Classify this cell by malaria status.
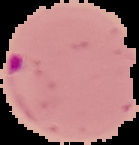

Parasitized.

{
  "image_size": "139×145 pixels",
  "preparation": "thin blood film",
  "image_type": "segmented cell region with the area outside set to black"
}